Locate malaria parasites and leukocytes.
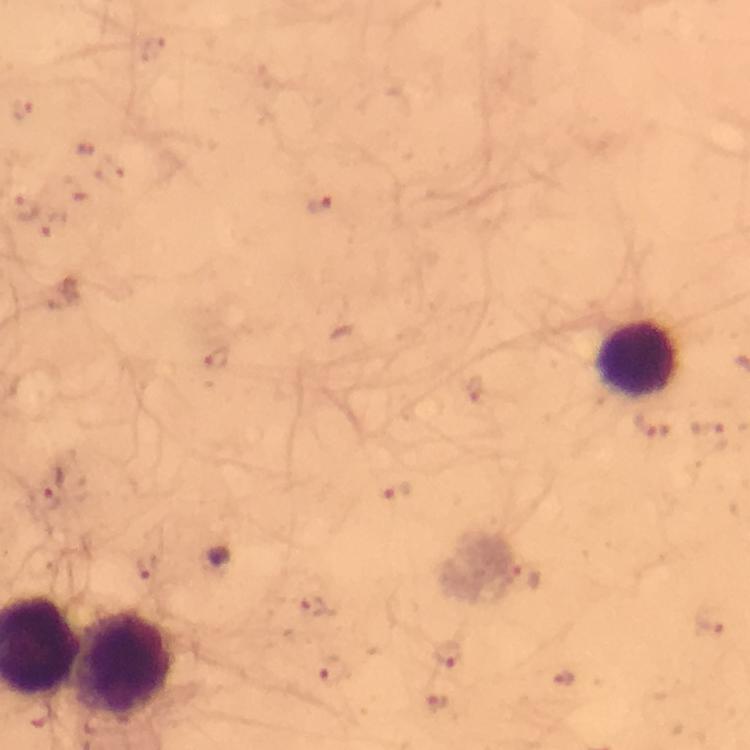
Approximate centers as {x, y} in pixels.
Malaria parasites: {319, 204}, {23, 205}, {55, 224}, {217, 358}, {652, 427}, {53, 485}, {398, 493}, {146, 566}, {525, 576}, {313, 605}, {446, 655}, {330, 671}, {564, 679}.
Leukocytes: {638, 359}, {126, 663}.

cropped from = a single field of view
magnification = 100x
preparation = thick blood film
image size = 750×750 pixels
stain = Giemsa
context = from a diagnostic examination for malaria
immersion oil = applied
capture = smartphone mounted on the microscope